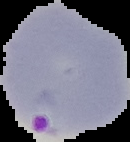

From a thin blood film. Malaria status: parasitized. Image is 130×142 pixels. Segmented cell region on a black background.